Classify this cell by malaria status.
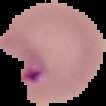
Parasitized.

From a thin blood smear. Image is 106×106 pixels. Segmented cell region on a black background.